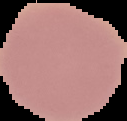

Malaria status: uninfected. From a thin blood smear. The area outside the segmented cell region is set to black. Image is 127×121 pixels.